Locate every uninfected red blood cell.
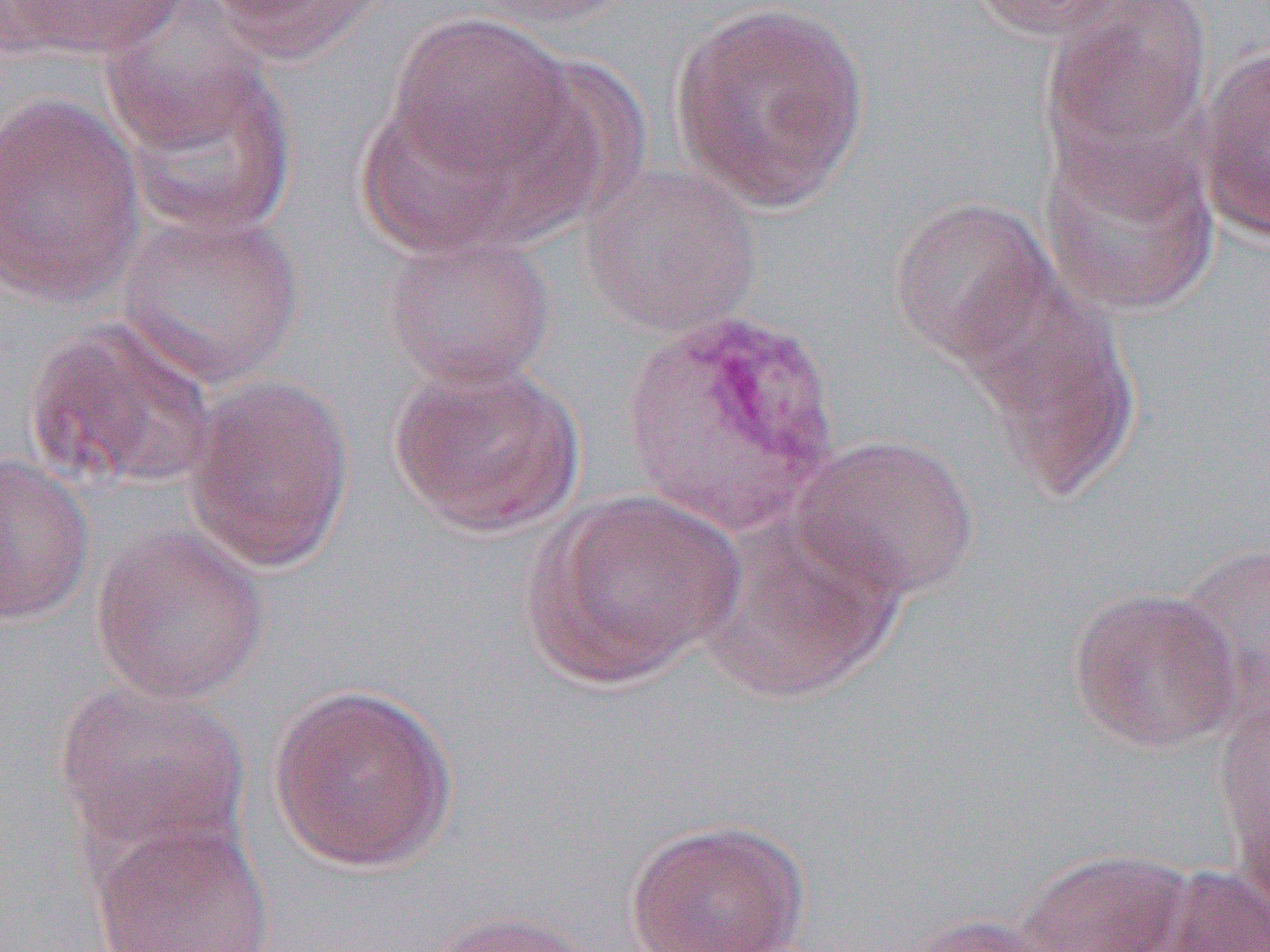
Approximate bounding boxes as named x1/y1/x2/y2 corners in pixels.
Uninfected red blood cells: (x1=8, y1=0, x2=189, y2=60), (x1=202, y1=0, x2=386, y2=67), (x1=460, y1=0, x2=637, y2=28), (x1=967, y1=0, x2=1136, y2=41), (x1=1041, y1=1, x2=1212, y2=179), (x1=669, y1=2, x2=871, y2=214), (x1=100, y1=7, x2=272, y2=154), (x1=383, y1=12, x2=581, y2=190), (x1=1194, y1=44, x2=1270, y2=241), (x1=115, y1=56, x2=298, y2=237), (x1=0, y1=91, x2=146, y2=309), (x1=353, y1=92, x2=526, y2=259), (x1=1039, y1=130, x2=1220, y2=317), (x1=580, y1=161, x2=762, y2=338), (x1=888, y1=195, x2=1060, y2=368), (x1=116, y1=209, x2=305, y2=389), (x1=381, y1=231, x2=557, y2=391), (x1=960, y1=280, x2=1142, y2=499), (x1=24, y1=317, x2=219, y2=493), (x1=388, y1=360, x2=585, y2=537), (x1=181, y1=374, x2=356, y2=574), (x1=791, y1=432, x2=980, y2=604), (x1=0, y1=455, x2=95, y2=625), (x1=525, y1=489, x2=746, y2=689), (x1=694, y1=512, x2=903, y2=704), (x1=89, y1=523, x2=271, y2=705), (x1=1172, y1=542, x2=1270, y2=712), (x1=1066, y1=586, x2=1242, y2=754), (x1=53, y1=677, x2=251, y2=867), (x1=266, y1=681, x2=460, y2=874), (x1=1235, y1=793, x2=1270, y2=940), (x1=623, y1=817, x2=812, y2=952), (x1=90, y1=818, x2=277, y2=952), (x1=1018, y1=848, x2=1192, y2=952), (x1=1150, y1=866, x2=1270, y2=952), (x1=422, y1=908, x2=599, y2=952), (x1=895, y1=913, x2=1067, y2=952).

slide-level diagnosis = Plasmodium vivax
modality = optical microscopy
magnification = 1000x
preparation = thin blood film
image size = 1270×952 pixels
field of view = one of a larger specimen